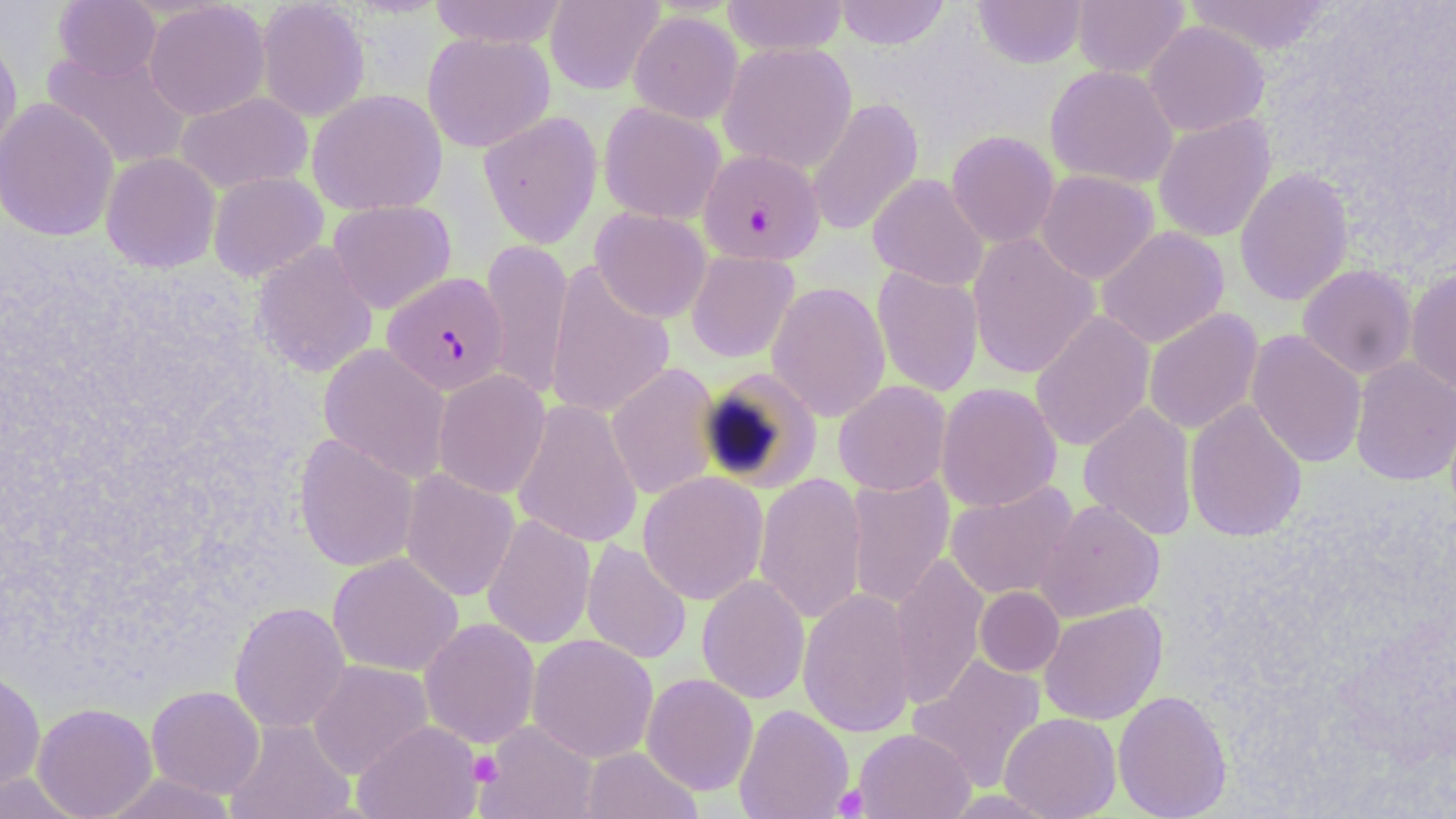

Approximate bounding boxes as named x1/y1/x2/y2 corners in pixels. Plasmodium falciparum-infected red blood cell locations: (x1=698, y1=148, x2=826, y2=266), (x1=382, y1=272, x2=510, y2=395). Uninfected red blood cell locations: (x1=428, y1=0, x2=570, y2=49), (x1=545, y1=0, x2=665, y2=95), (x1=722, y1=0, x2=848, y2=56), (x1=834, y1=0, x2=950, y2=49), (x1=973, y1=0, x2=1087, y2=68), (x1=1072, y1=0, x2=1189, y2=79), (x1=1184, y1=0, x2=1336, y2=56), (x1=54, y1=1, x2=161, y2=81), (x1=144, y1=1, x2=270, y2=120), (x1=256, y1=1, x2=371, y2=122), (x1=628, y1=11, x2=743, y2=124), (x1=1143, y1=20, x2=1269, y2=137), (x1=0, y1=30, x2=23, y2=169), (x1=422, y1=32, x2=555, y2=152), (x1=719, y1=42, x2=857, y2=173), (x1=42, y1=49, x2=192, y2=170), (x1=1044, y1=64, x2=1179, y2=189), (x1=308, y1=89, x2=447, y2=216), (x1=175, y1=91, x2=313, y2=194), (x1=0, y1=97, x2=120, y2=242), (x1=806, y1=97, x2=924, y2=237), (x1=598, y1=102, x2=726, y2=225), (x1=478, y1=111, x2=602, y2=249), (x1=1153, y1=114, x2=1276, y2=243), (x1=946, y1=130, x2=1060, y2=249), (x1=101, y1=152, x2=220, y2=272), (x1=1234, y1=166, x2=1355, y2=306), (x1=1035, y1=169, x2=1159, y2=284), (x1=208, y1=171, x2=328, y2=281), (x1=868, y1=174, x2=989, y2=291), (x1=328, y1=200, x2=456, y2=314), (x1=590, y1=208, x2=712, y2=323), (x1=1096, y1=225, x2=1229, y2=349), (x1=966, y1=232, x2=1100, y2=379), (x1=479, y1=238, x2=573, y2=401), (x1=251, y1=241, x2=379, y2=378), (x1=686, y1=250, x2=799, y2=363), (x1=545, y1=261, x2=675, y2=421), (x1=1297, y1=264, x2=1418, y2=380), (x1=872, y1=266, x2=984, y2=398), (x1=1405, y1=266, x2=1456, y2=395), (x1=767, y1=281, x2=890, y2=422), (x1=1143, y1=308, x2=1263, y2=435), (x1=1029, y1=310, x2=1155, y2=451), (x1=1246, y1=329, x2=1367, y2=469), (x1=318, y1=344, x2=451, y2=483), (x1=1350, y1=356, x2=1456, y2=486), (x1=606, y1=362, x2=722, y2=501), (x1=700, y1=366, x2=824, y2=493), (x1=433, y1=370, x2=551, y2=499), (x1=833, y1=380, x2=952, y2=496), (x1=936, y1=382, x2=1062, y2=513), (x1=512, y1=399, x2=643, y2=549), (x1=1184, y1=399, x2=1307, y2=542), (x1=1078, y1=402, x2=1197, y2=541), (x1=294, y1=433, x2=418, y2=572), (x1=400, y1=469, x2=520, y2=602), (x1=638, y1=471, x2=768, y2=605), (x1=753, y1=472, x2=868, y2=625), (x1=845, y1=473, x2=954, y2=610), (x1=945, y1=481, x2=1079, y2=600), (x1=1036, y1=499, x2=1165, y2=622), (x1=482, y1=514, x2=596, y2=649), (x1=581, y1=539, x2=692, y2=665), (x1=890, y1=551, x2=989, y2=711), (x1=327, y1=553, x2=463, y2=676), (x1=696, y1=574, x2=811, y2=705), (x1=798, y1=586, x2=917, y2=739), (x1=974, y1=586, x2=1064, y2=677), (x1=229, y1=601, x2=351, y2=734), (x1=1039, y1=601, x2=1167, y2=725), (x1=419, y1=618, x2=540, y2=749), (x1=527, y1=633, x2=658, y2=763), (x1=909, y1=654, x2=1047, y2=792), (x1=308, y1=660, x2=433, y2=779), (x1=0, y1=667, x2=46, y2=795), (x1=641, y1=673, x2=758, y2=795), (x1=146, y1=685, x2=265, y2=798), (x1=1112, y1=689, x2=1232, y2=819), (x1=32, y1=702, x2=158, y2=818), (x1=734, y1=704, x2=853, y2=819), (x1=999, y1=712, x2=1122, y2=819), (x1=225, y1=718, x2=356, y2=819), (x1=353, y1=720, x2=484, y2=819), (x1=477, y1=721, x2=600, y2=819), (x1=853, y1=728, x2=975, y2=819), (x1=580, y1=746, x2=702, y2=819), (x1=0, y1=771, x2=84, y2=818), (x1=98, y1=772, x2=238, y2=819). Platelet locations: (x1=469, y1=750, x2=503, y2=785), (x1=833, y1=784, x2=869, y2=817). Slide-level diagnosis: Plasmodium falciparum. May-Grünwald-Giemsa-stained preparation. Image is 1456×819 pixels. Captured at 1000x magnification. Optical microscopy. Thin blood smear. Single field of view.